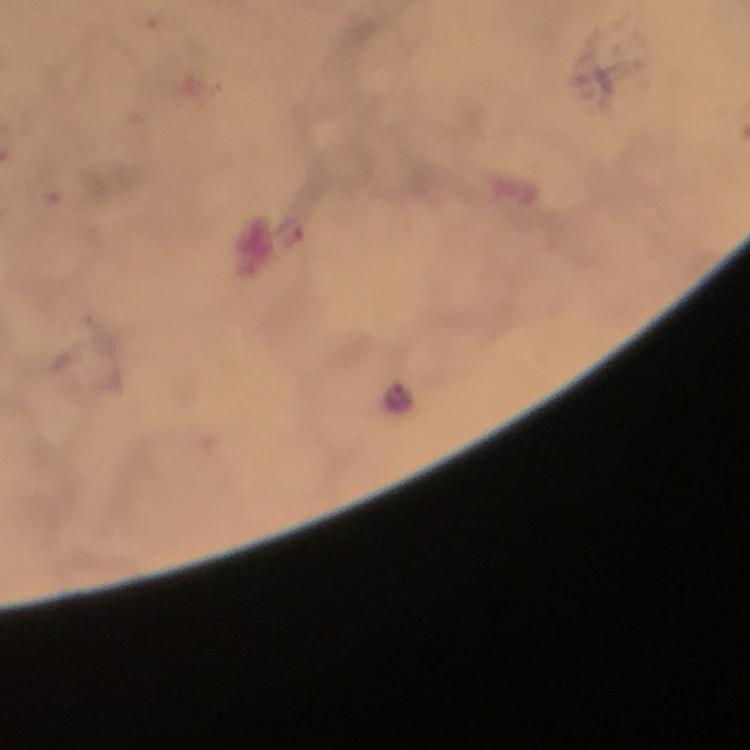
image_size: 750×750 pixels
stain: Giemsa
preparation: thick blood film
magnification: 100x
context: from a diagnostic examination for malaria
capture: smartphone photograph through a microscope
malaria_parasite_locations: 'approximate centers as [x, y] in pixels: [400, 400]'
cropped_from: a single field of view
immersion_oil: applied